State the blood parasite species.
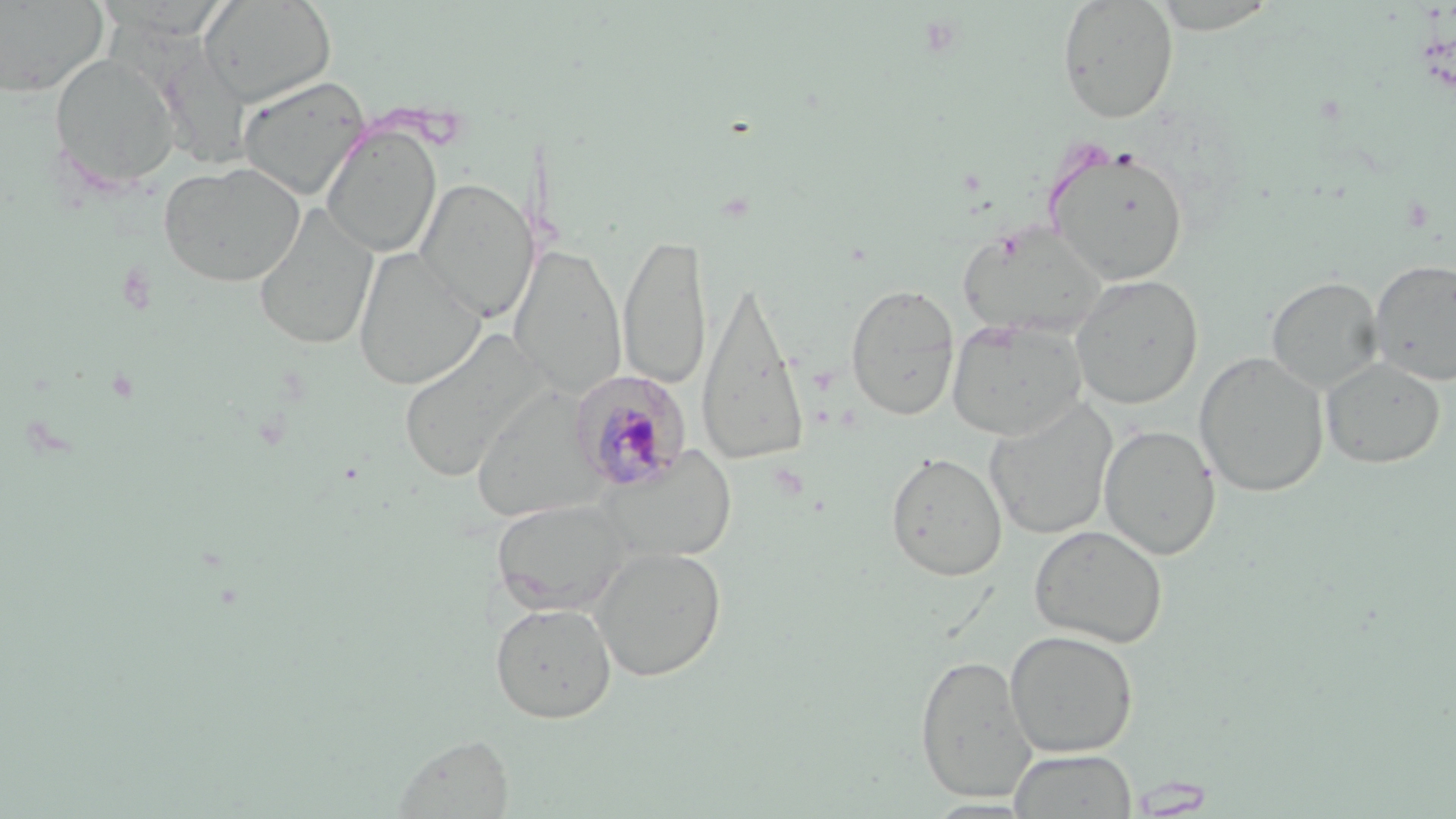

Plasmodium malariae.

Summary:
  - Coordinate format: approximate bounding boxes as [x1, y1, x2, y2] in pixels
  - Plasmodium malariae-infected red blood cell locations: [568, 369, 692, 493]
  - Uninfected red blood cell locations: [199, 0, 337, 106], [1057, 0, 1179, 124], [0, 1, 108, 97], [48, 53, 181, 192], [237, 75, 370, 201], [321, 122, 442, 258], [1045, 145, 1189, 286], [158, 162, 306, 287], [415, 177, 539, 322], [254, 203, 378, 351], [958, 224, 1109, 340], [618, 232, 712, 391], [509, 245, 628, 396], [353, 248, 486, 391], [1369, 259, 1456, 385], [1070, 274, 1204, 409], [1266, 276, 1383, 394], [696, 283, 812, 469], [845, 283, 960, 421], [947, 317, 1088, 441], [398, 329, 546, 484], [1194, 351, 1329, 497], [1320, 357, 1445, 469], [471, 382, 603, 524], [984, 398, 1118, 541], [1099, 424, 1220, 560], [599, 446, 738, 563], [885, 451, 1008, 581], [492, 499, 628, 614], [1028, 524, 1168, 648], [590, 546, 727, 681], [490, 601, 616, 723], [1004, 629, 1139, 758], [915, 654, 1037, 801], [393, 734, 515, 817], [1009, 749, 1137, 818]
  - Preparation: thin blood smear
  - Image size: 1456×819 pixels
  - Magnification: 1000x
  - Field of view: single
  - Modality: optical microscopy
  - Stain: May-Grünwald-Giemsa